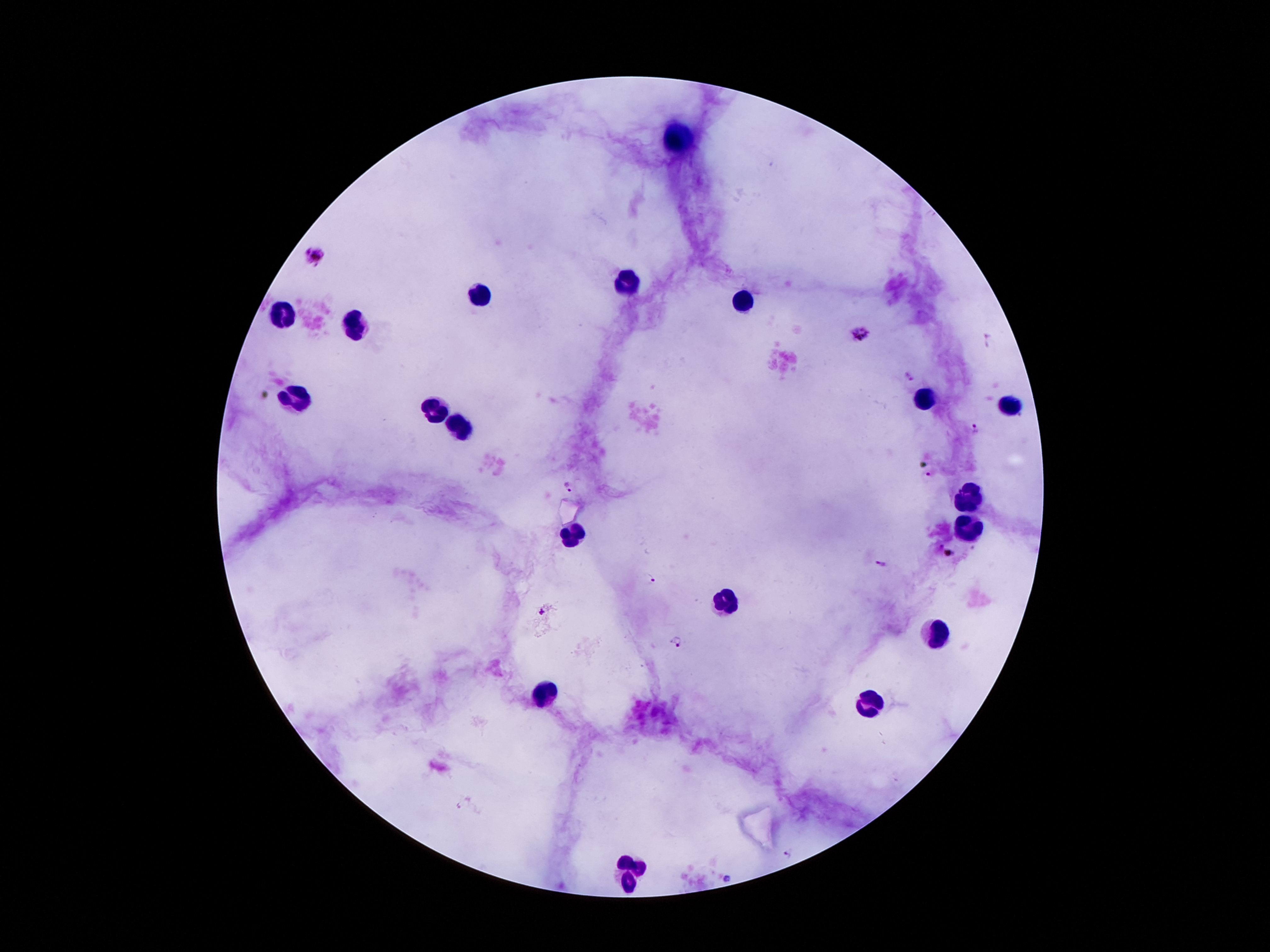 Thick blood smear. Image is 1270×952 pixels. Single field of view. Giemsa-stained preparation. Patient malaria status: positive for Plasmodium falciparum. 100x magnification. Smartphone photograph taken through the microscope eyepiece.